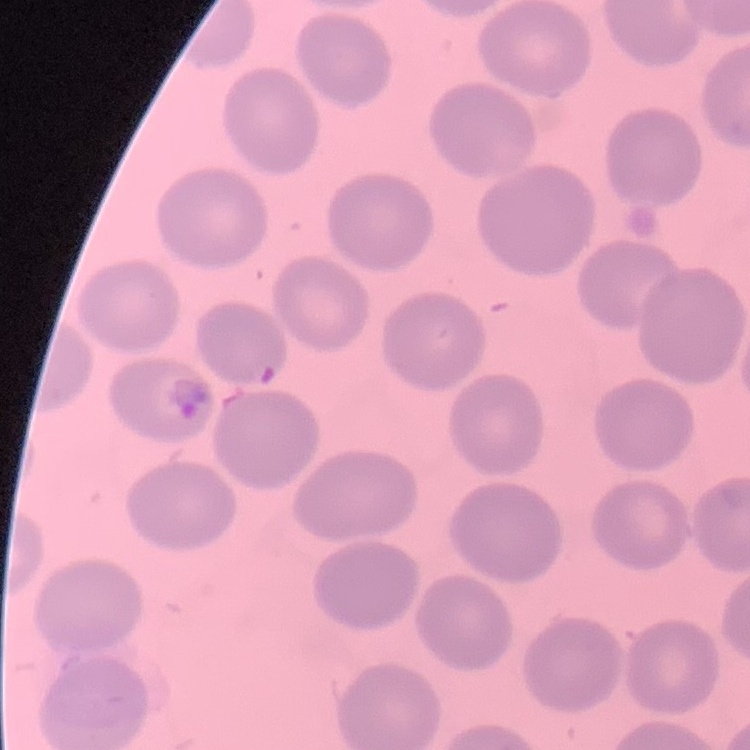 The erythrocytes show no rouleaux formation. Field's or Giemsa stain. Square crop of a larger photomicrograph. Thin blood film.